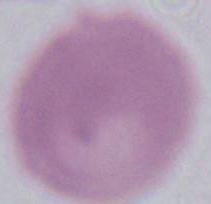 Photomicrograph. A red blood cell is seen. 1000x magnification.